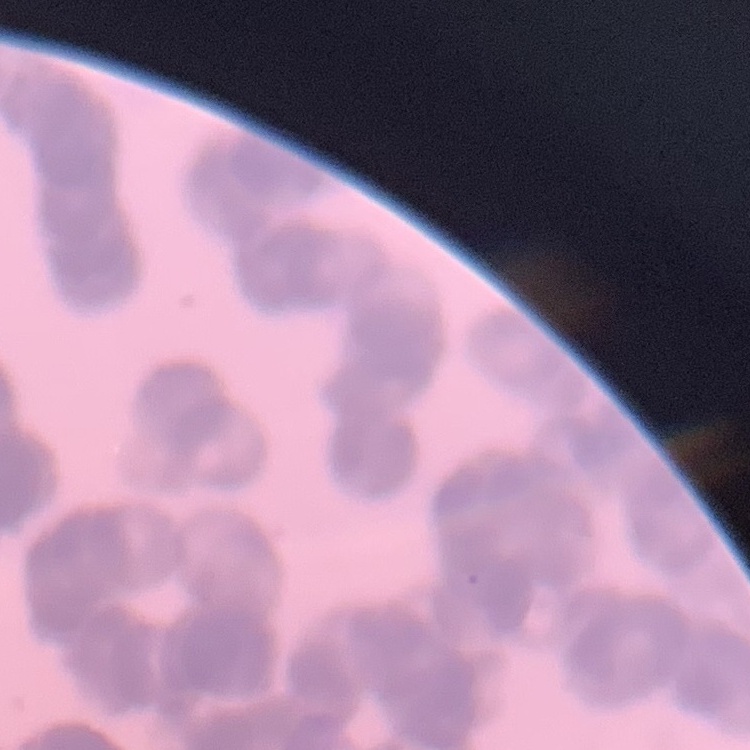
{
  "red_blood_cell_morphology": "rouleaux formation",
  "image_type": "square crop of a larger photomicrograph",
  "stain": "Field's or Giemsa",
  "preparation": "thin peripheral smear"
}